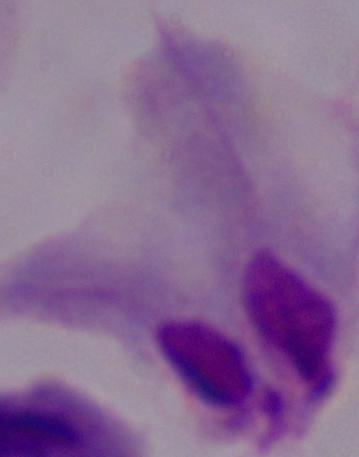
Summary:
  - Magnification: 1000x
  - Modality: micrograph
  - Identification: trichomonad